Report the malaria status of this cell.
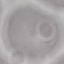

Uninfected.

Summary:
  - Image type: cell patch, automatically extracted from a larger field of view and resized to 64 × 64 pixels
  - Stain: Giemsa
  - Preparation: thin smear
  - Capture: smartphone through the microscope eyepiece